Give the position of every Plasmodium parasite visible.
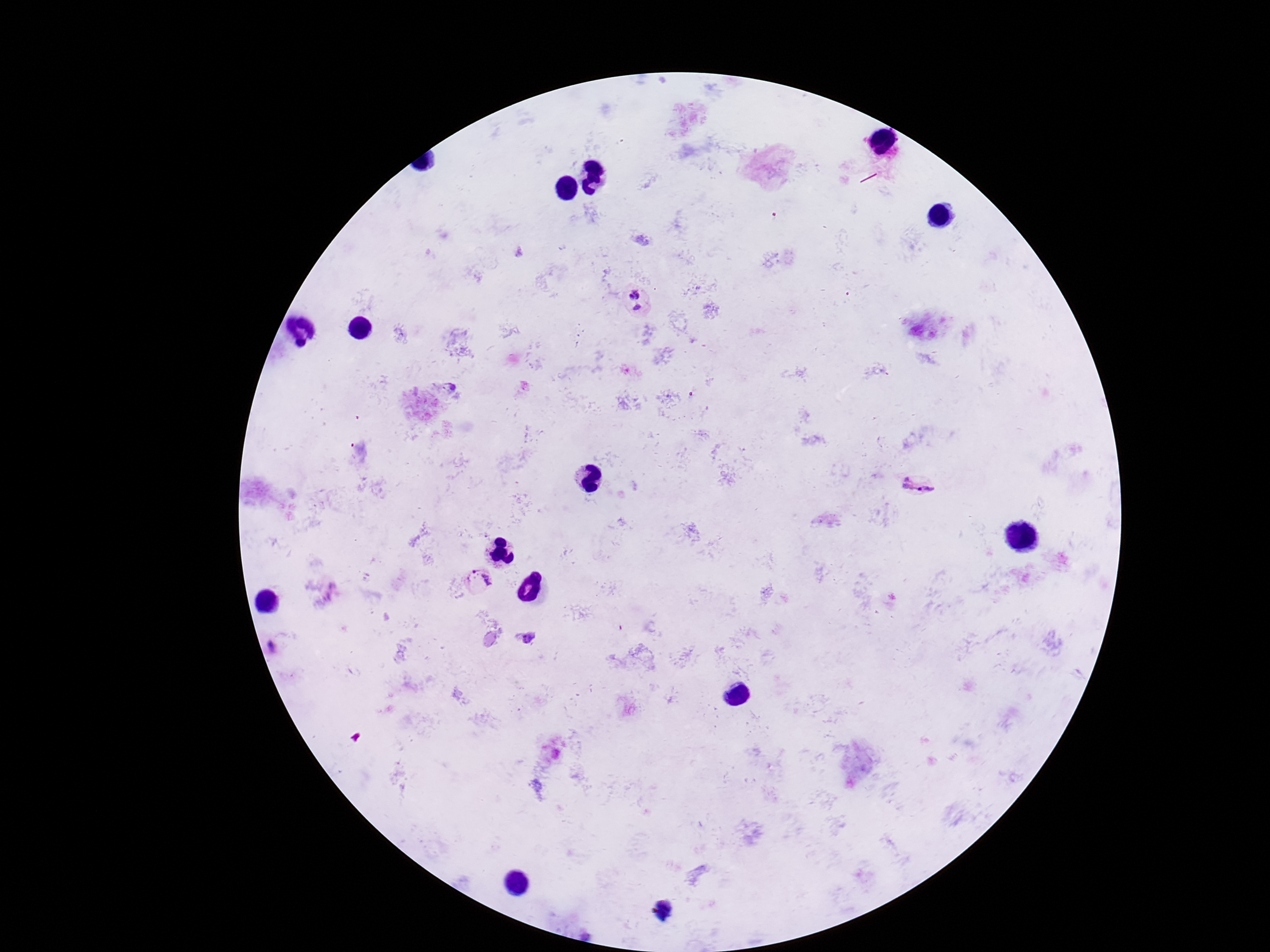
Approximate centers as (x, y) in pixels.
Plasmodium parasites: (633, 302), (918, 484), (479, 582), (529, 638), (662, 909).

Thick blood film. Photographed through the microscope eyepiece with a smartphone camera. Single field of view. Image is 1270×952 pixels. Giemsa-stained preparation. 100x magnification. Patient malaria status: positive.